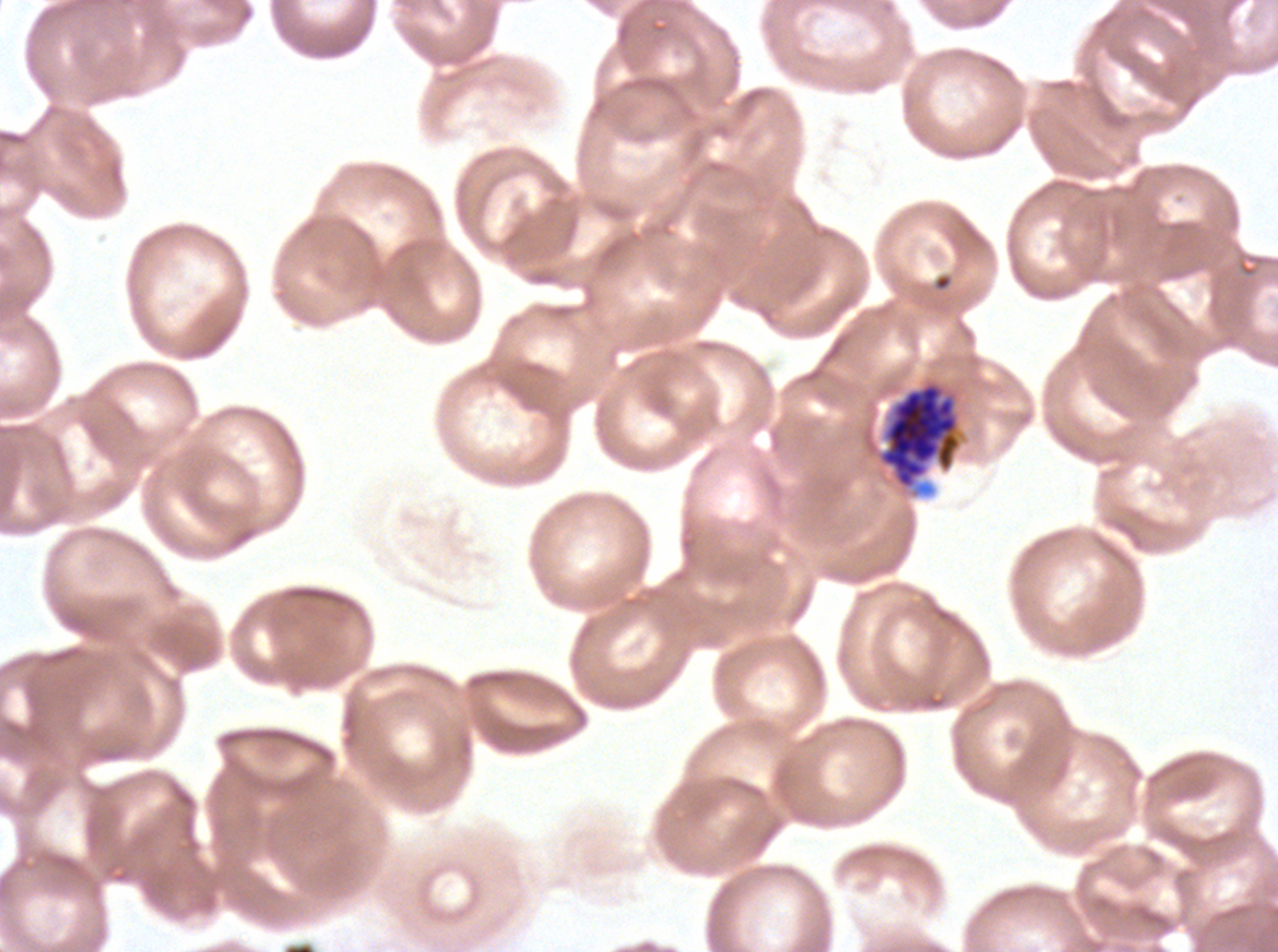

notation = approximate bounding boxes as {x1, y1, x2, y2} in pixels
late schizont locations = {878, 381, 962, 490}
preparation = thin blood film
specimen = P. falciparum from a patient in The Gambia, cultured ex vivo for 24 to 48 hours
image size = 1278×952 pixels
field of view = one sub-image of a larger composite
stain = Giemsa